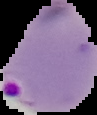 Image is 97×115 pixels. Result: malaria parasites identified. Cell region segmented out of the field of view; the surrounding area is masked to black. From a thin blood film.